Locate every blood parasite and identify its species.
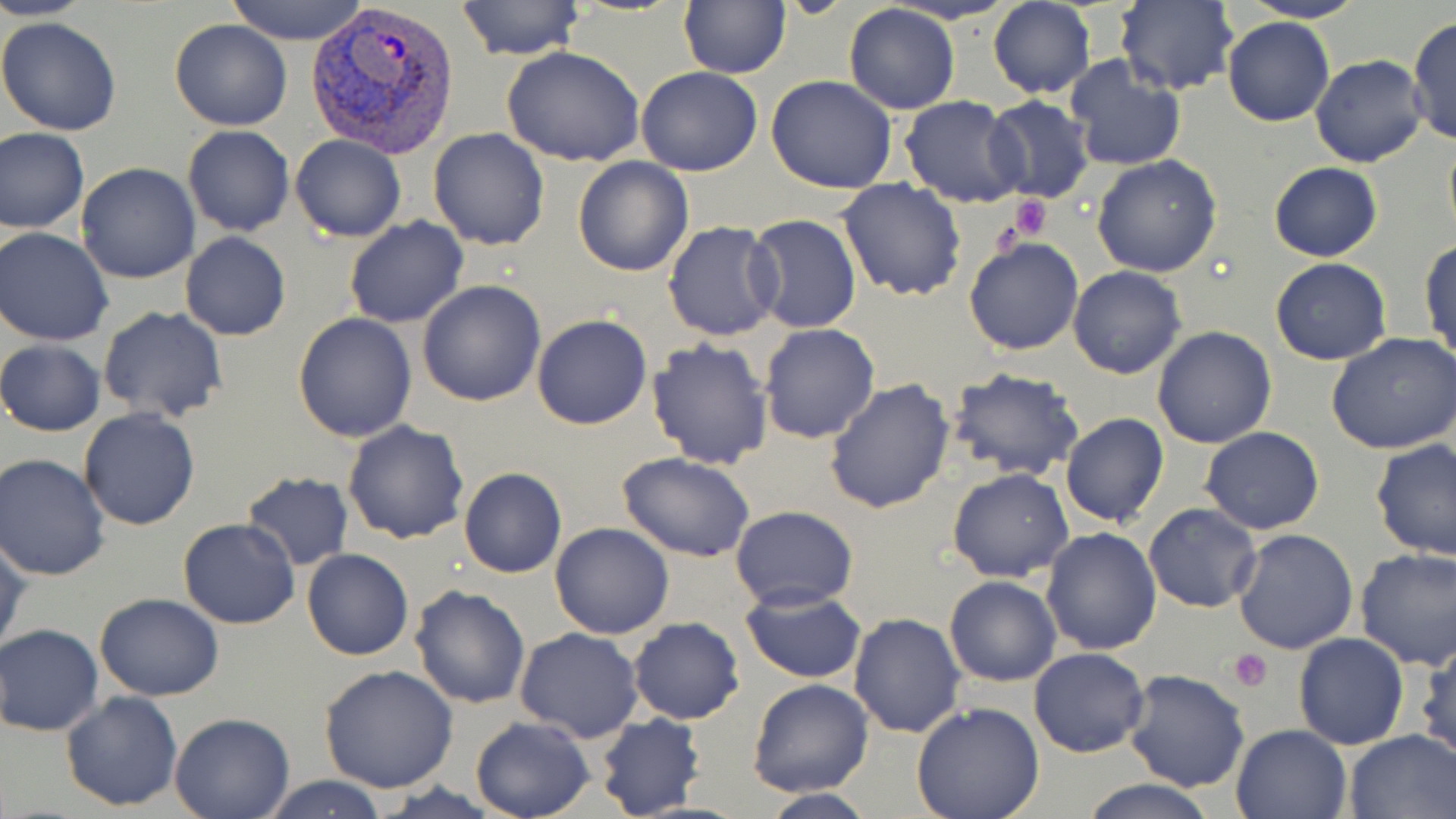
Approximate bounding boxes as named x1/y1/x2/y2 corners in pixels.
Plasmodium vivax-infected red blood cells: (x1=305, y1=0, x2=462, y2=158).
No Plasmodium falciparum, Plasmodium ovale, Plasmodium malariae, Babesia divergens, or Trypanosoma brucei observed.

Platelet locations: (x1=1010, y1=195, x2=1054, y2=240), (x1=990, y1=218, x2=1024, y2=258), (x1=1227, y1=648, x2=1273, y2=691). Uninfected red blood cell locations: (x1=0, y1=0, x2=93, y2=21), (x1=225, y1=0, x2=371, y2=44), (x1=455, y1=0, x2=585, y2=62), (x1=1236, y1=0, x2=1370, y2=23), (x1=678, y1=1, x2=790, y2=78), (x1=988, y1=1, x2=1094, y2=98), (x1=1115, y1=1, x2=1237, y2=95), (x1=843, y1=3, x2=960, y2=114), (x1=1407, y1=13, x2=1456, y2=149), (x1=0, y1=15, x2=123, y2=138), (x1=1223, y1=16, x2=1335, y2=127), (x1=170, y1=18, x2=292, y2=130), (x1=500, y1=45, x2=646, y2=168), (x1=1064, y1=55, x2=1186, y2=172), (x1=1310, y1=55, x2=1429, y2=168), (x1=637, y1=66, x2=763, y2=177), (x1=766, y1=74, x2=898, y2=193), (x1=982, y1=95, x2=1097, y2=203), (x1=899, y1=96, x2=1027, y2=207), (x1=182, y1=125, x2=295, y2=237), (x1=0, y1=127, x2=89, y2=234), (x1=428, y1=129, x2=549, y2=250), (x1=1443, y1=129, x2=1456, y2=247), (x1=289, y1=135, x2=406, y2=243), (x1=1092, y1=156, x2=1223, y2=278), (x1=573, y1=157, x2=693, y2=277), (x1=76, y1=163, x2=200, y2=283), (x1=1268, y1=163, x2=1383, y2=261), (x1=837, y1=178, x2=967, y2=302), (x1=748, y1=214, x2=862, y2=333), (x1=344, y1=217, x2=469, y2=328), (x1=662, y1=221, x2=783, y2=340), (x1=1, y1=228, x2=117, y2=346), (x1=180, y1=232, x2=291, y2=342), (x1=964, y1=236, x2=1084, y2=355), (x1=1421, y1=238, x2=1455, y2=370), (x1=1270, y1=258, x2=1394, y2=365), (x1=1068, y1=266, x2=1186, y2=379), (x1=417, y1=280, x2=548, y2=406), (x1=98, y1=306, x2=228, y2=424), (x1=294, y1=313, x2=417, y2=442), (x1=531, y1=314, x2=653, y2=431), (x1=759, y1=323, x2=881, y2=443), (x1=1152, y1=326, x2=1277, y2=448), (x1=1327, y1=334, x2=1456, y2=455), (x1=646, y1=337, x2=775, y2=467), (x1=0, y1=339, x2=105, y2=438), (x1=945, y1=366, x2=1086, y2=482), (x1=824, y1=378, x2=956, y2=513), (x1=78, y1=409, x2=202, y2=531), (x1=1060, y1=411, x2=1170, y2=527), (x1=342, y1=420, x2=470, y2=544), (x1=1199, y1=426, x2=1324, y2=534), (x1=1370, y1=437, x2=1456, y2=558), (x1=617, y1=453, x2=757, y2=563), (x1=0, y1=454, x2=109, y2=581), (x1=458, y1=466, x2=566, y2=579), (x1=947, y1=467, x2=1075, y2=582), (x1=240, y1=471, x2=355, y2=571), (x1=1142, y1=502, x2=1263, y2=614), (x1=730, y1=505, x2=857, y2=610), (x1=178, y1=518, x2=302, y2=631), (x1=550, y1=522, x2=674, y2=639), (x1=1041, y1=528, x2=1162, y2=655), (x1=1232, y1=528, x2=1359, y2=654), (x1=0, y1=532, x2=28, y2=658), (x1=1354, y1=547, x2=1456, y2=670), (x1=302, y1=548, x2=415, y2=661), (x1=943, y1=575, x2=1062, y2=686), (x1=408, y1=584, x2=531, y2=709), (x1=740, y1=585, x2=868, y2=683), (x1=95, y1=593, x2=224, y2=700), (x1=848, y1=612, x2=966, y2=738), (x1=628, y1=617, x2=745, y2=725), (x1=0, y1=623, x2=104, y2=736), (x1=514, y1=627, x2=644, y2=743), (x1=1293, y1=632, x2=1409, y2=749), (x1=1416, y1=636, x2=1455, y2=768), (x1=1028, y1=647, x2=1150, y2=759), (x1=318, y1=665, x2=460, y2=793), (x1=1122, y1=668, x2=1252, y2=792), (x1=748, y1=679, x2=874, y2=798), (x1=60, y1=691, x2=184, y2=810), (x1=911, y1=701, x2=1045, y2=819), (x1=594, y1=712, x2=706, y2=819), (x1=169, y1=713, x2=294, y2=819), (x1=469, y1=716, x2=597, y2=819), (x1=1229, y1=723, x2=1352, y2=817), (x1=1344, y1=728, x2=1456, y2=818), (x1=259, y1=775, x2=392, y2=818), (x1=1077, y1=779, x2=1222, y2=819), (x1=755, y1=789, x2=878, y2=818). Slide-level diagnosis: Plasmodium vivax. May-Grünwald-Giemsa-stained preparation. Image is 1456×819 pixels. Captured at 1000x magnification. Optical microscopy. Thin blood smear. One field of a larger specimen.